State which cell type is depicted.
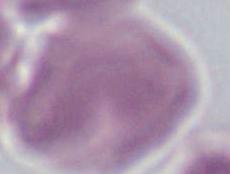
This is an erythrocyte.

{
  "modality": "photomicrograph",
  "magnification": "1000x"
}